Assess this cell for malaria.
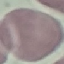
It is uninfected.

capture: smartphone through the microscope eyepiece
preparation: thin smear
image_type: automatically extracted cell patch, resized to 64 × 64 pixels
stain: Giemsa